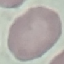 Malaria status: uninfected. Cell patch, automatically extracted from a larger field of view and resized to 64 × 64 pixels. Giemsa stain. Thin smear of blood. Photographed with a smartphone camera at the microscope eyepiece.